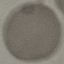
Malaria status: uninfected. Giemsa-stained preparation. Automatically extracted cell patch, resized to 64 × 64 pixels. Thin smear of blood. Acquired by smartphone through the microscope eyepiece.